Assess the morphology of the red blood cells.
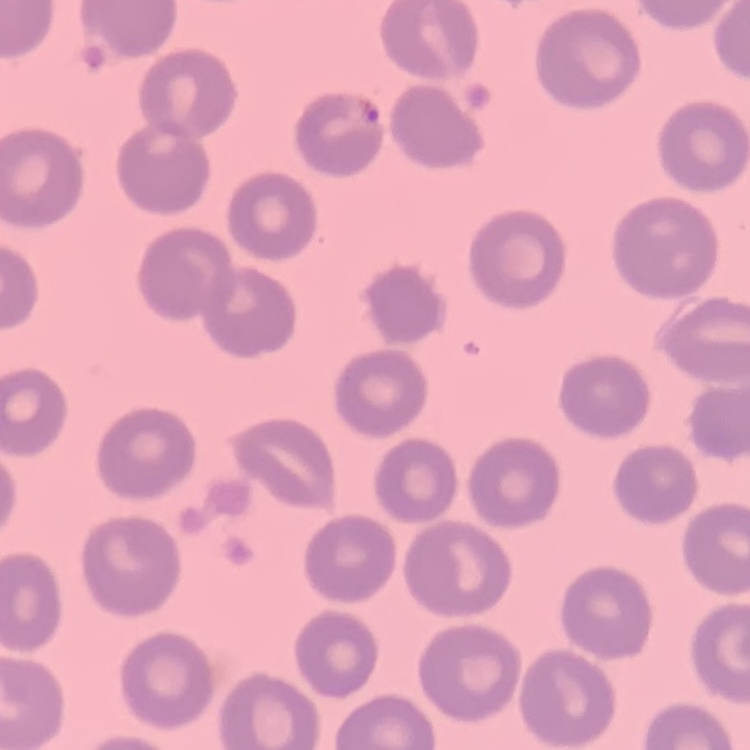
No rouleaux formation.

image_type: square crop of a larger photomicrograph
preparation: thin peripheral smear
stain: Field's or Giemsa